Locate every malaria parasite.
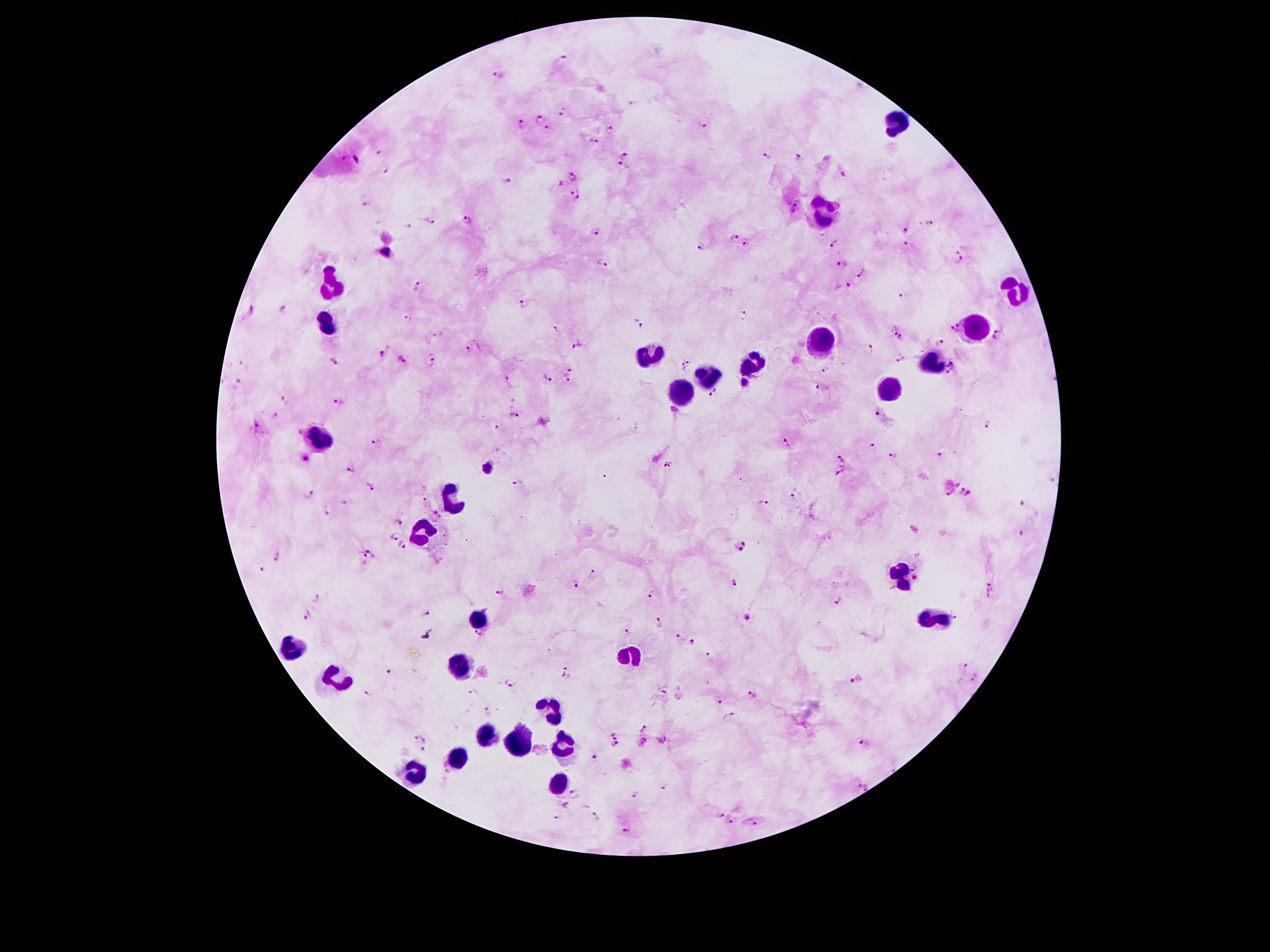

Approximate centers as [x, y] in pixels.
Malaria parasites: [561, 58], [500, 74], [562, 112], [541, 119], [703, 124], [522, 125], [548, 130], [610, 130], [594, 141], [377, 153], [624, 154], [768, 157], [345, 158], [799, 158], [624, 168], [388, 172], [571, 175], [506, 182], [557, 184], [574, 189], [578, 200], [366, 205], [793, 208], [429, 220], [467, 221], [929, 222], [595, 229], [908, 229], [734, 237], [747, 244], [834, 244], [905, 245], [703, 246], [961, 249], [386, 253], [959, 261], [603, 263], [841, 264], [861, 274], [418, 286], [844, 287], [900, 296], [521, 303], [283, 309], [253, 311], [746, 313], [409, 320], [635, 325], [952, 327], [555, 330], [892, 331], [998, 335], [902, 339], [940, 342], [577, 345], [868, 348], [467, 350], [380, 355], [401, 359], [900, 359], [333, 361], [432, 361], [686, 364], [824, 369], [953, 369], [571, 371], [547, 378], [237, 380], [506, 380], [566, 380], [745, 383], [819, 387], [715, 393], [285, 400], [340, 401], [673, 412], [876, 412], [275, 415], [514, 416], [987, 424], [256, 427], [300, 433], [376, 442], [786, 444], [874, 446], [940, 455], [844, 456], [894, 456], [306, 460], [667, 465], [351, 468], [487, 468], [841, 471], [518, 482], [369, 486], [960, 491], [950, 493], [307, 494], [969, 494], [792, 496], [425, 500], [763, 502], [327, 510], [436, 511], [398, 522], [395, 535], [1024, 535], [745, 542], [403, 545], [740, 550], [372, 551], [919, 553], [278, 557], [365, 560], [593, 571], [575, 583], [734, 583], [992, 586], [500, 593], [651, 594], [316, 598], [839, 602], [425, 612], [307, 614], [745, 619], [659, 622], [628, 632], [677, 637], [691, 644], [707, 655], [964, 667], [566, 671], [389, 672], [974, 678], [856, 679], [510, 683], [665, 690], [474, 691], [368, 693], [752, 696], [719, 702], [487, 711], [729, 716], [644, 730], [614, 734], [421, 736], [663, 741], [863, 744], [615, 747], [425, 750], [594, 757], [855, 784], [664, 787], [867, 787], [575, 793], [636, 795], [566, 804], [720, 815], [597, 816], [557, 817], [731, 822], [756, 824], [627, 830].

Summary:
  - Leukocyte locations: [896, 120], [821, 214], [331, 286], [1021, 290], [325, 322], [974, 329], [816, 343], [649, 355], [933, 361], [751, 363], [708, 374], [681, 388], [890, 388], [321, 439], [452, 499], [421, 533], [902, 574], [933, 617], [477, 622], [628, 656], [462, 661], [550, 706], [487, 736], [565, 742], [519, 745], [456, 753], [413, 773], [560, 786]
  - Field of view: single
  - Magnification: 100x
  - Capture: smartphone through the microscope eyepiece
  - Patient malaria status: infected with Plasmodium falciparum
  - Image size: 1270×952 pixels
  - Preparation: thick peripheral-blood smear
  - Stain: Giemsa